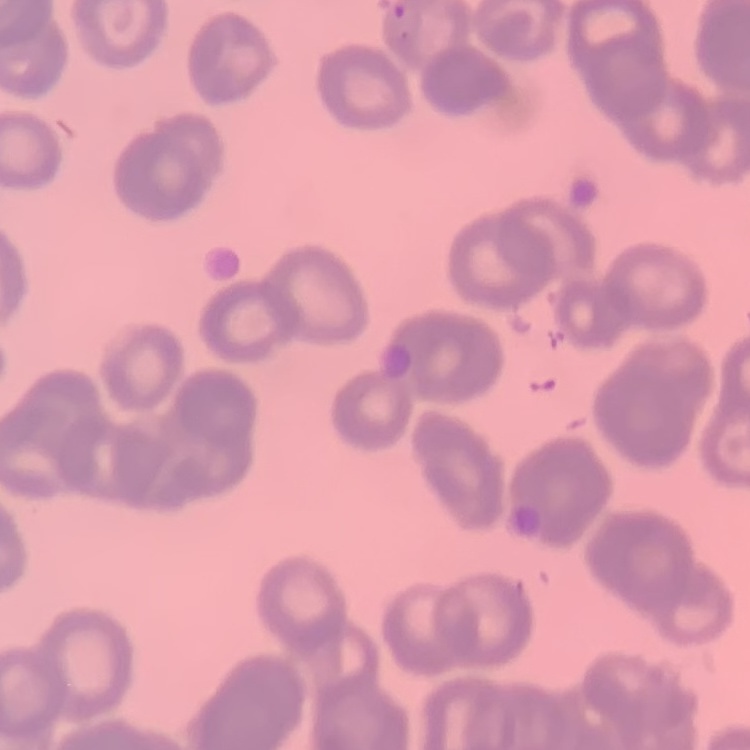

red blood cell morphology = rouleaux formation
stain = Field's or Giemsa
preparation = thin blood film
image type = square crop of a larger photomicrograph